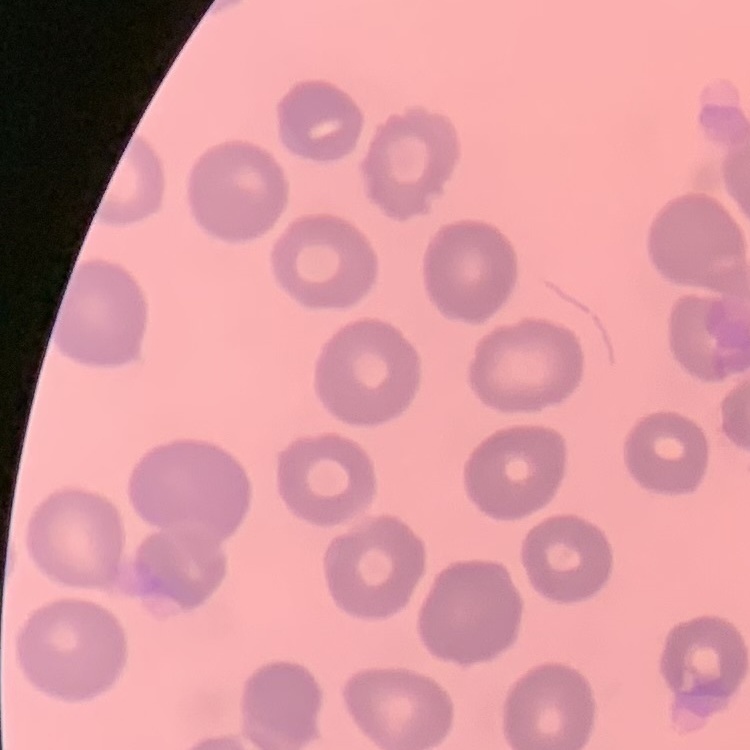
The red blood cells show no rouleaux formation. Thin blood smear. Field's or Giemsa stain. One tile cut from a larger photomicrograph.